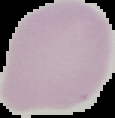

result = negative for malaria parasites
image type = segmented cell region with the area outside set to black
preparation = thin blood smear
image size = 115×118 pixels